Locate and identify every blood parasite.
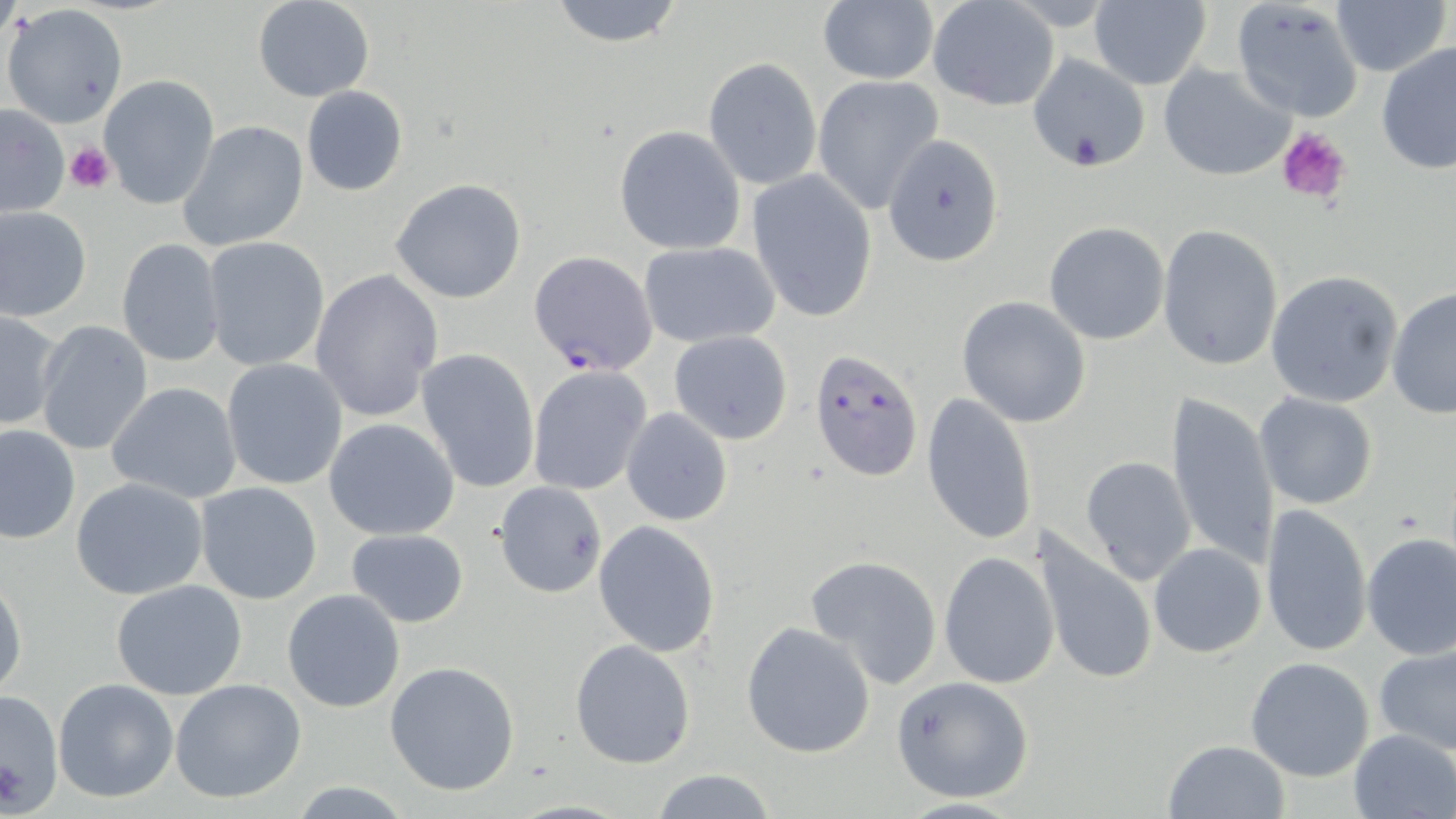
Approximate bounding boxes as named x1/y1/x2/y2 corners in pixels.
Plasmodium falciparum-infected red blood cells: (x1=529, y1=250, x2=657, y2=376), (x1=810, y1=349, x2=924, y2=481).
No Plasmodium ovale, Plasmodium malariae, Plasmodium vivax, Babesia divergens, or Trypanosoma brucei observed.

Summary:
  - Uninfected red blood cell locations: (x1=548, y1=0, x2=686, y2=48), (x1=818, y1=0, x2=938, y2=86), (x1=1231, y1=0, x2=1364, y2=123), (x1=251, y1=1, x2=375, y2=102), (x1=1086, y1=1, x2=1211, y2=89), (x1=1334, y1=1, x2=1447, y2=77), (x1=926, y1=3, x2=1060, y2=112), (x1=1, y1=4, x2=129, y2=129), (x1=1376, y1=42, x2=1456, y2=174), (x1=1028, y1=52, x2=1154, y2=175), (x1=704, y1=58, x2=822, y2=190), (x1=1158, y1=62, x2=1297, y2=182), (x1=819, y1=67, x2=951, y2=207), (x1=98, y1=75, x2=219, y2=211), (x1=300, y1=86, x2=407, y2=197), (x1=0, y1=105, x2=70, y2=218), (x1=178, y1=121, x2=309, y2=253), (x1=613, y1=125, x2=746, y2=255), (x1=882, y1=135, x2=1006, y2=266), (x1=746, y1=170, x2=878, y2=323), (x1=390, y1=178, x2=529, y2=304), (x1=0, y1=205, x2=91, y2=321), (x1=1044, y1=222, x2=1170, y2=345), (x1=1157, y1=224, x2=1284, y2=372), (x1=202, y1=236, x2=329, y2=371), (x1=117, y1=238, x2=224, y2=366), (x1=638, y1=241, x2=780, y2=349), (x1=309, y1=267, x2=444, y2=421), (x1=1266, y1=270, x2=1403, y2=408), (x1=1387, y1=285, x2=1456, y2=419), (x1=955, y1=296, x2=1092, y2=428), (x1=0, y1=310, x2=62, y2=431), (x1=34, y1=321, x2=152, y2=457), (x1=668, y1=330, x2=794, y2=445), (x1=416, y1=348, x2=540, y2=493), (x1=221, y1=359, x2=349, y2=488), (x1=527, y1=365, x2=652, y2=495), (x1=104, y1=381, x2=243, y2=503), (x1=1166, y1=391, x2=1280, y2=570), (x1=1254, y1=393, x2=1379, y2=510), (x1=921, y1=394, x2=1036, y2=548), (x1=621, y1=408, x2=732, y2=526), (x1=323, y1=418, x2=460, y2=539), (x1=0, y1=424, x2=79, y2=543), (x1=1080, y1=455, x2=1196, y2=583), (x1=71, y1=478, x2=210, y2=601), (x1=195, y1=482, x2=324, y2=605), (x1=493, y1=482, x2=608, y2=598), (x1=1260, y1=502, x2=1373, y2=657), (x1=593, y1=519, x2=720, y2=657), (x1=1035, y1=527, x2=1158, y2=690), (x1=346, y1=528, x2=470, y2=628), (x1=1361, y1=532, x2=1456, y2=660), (x1=1148, y1=543, x2=1265, y2=660), (x1=938, y1=551, x2=1057, y2=689), (x1=806, y1=555, x2=943, y2=688), (x1=1, y1=574, x2=27, y2=700), (x1=111, y1=580, x2=248, y2=701), (x1=282, y1=588, x2=406, y2=713), (x1=741, y1=621, x2=875, y2=757), (x1=570, y1=638, x2=696, y2=768), (x1=1374, y1=646, x2=1456, y2=756), (x1=1245, y1=657, x2=1375, y2=782), (x1=385, y1=661, x2=520, y2=796), (x1=891, y1=675, x2=1036, y2=803), (x1=52, y1=678, x2=179, y2=804), (x1=170, y1=678, x2=306, y2=804), (x1=1, y1=690, x2=65, y2=811), (x1=1349, y1=728, x2=1455, y2=817), (x1=1162, y1=739, x2=1290, y2=818), (x1=647, y1=767, x2=778, y2=819), (x1=891, y1=797, x2=1030, y2=818)
  - Platelet locations: (x1=1274, y1=125, x2=1354, y2=206), (x1=65, y1=143, x2=115, y2=194), (x1=0, y1=754, x2=24, y2=812)
  - Slide-level diagnosis: Plasmodium falciparum
  - Magnification: 1000x
  - Field of view: single
  - Modality: light microscopy
  - Preparation: thin blood smear
  - Stain: May-Grünwald-Giemsa
  - Image size: 1456×819 pixels